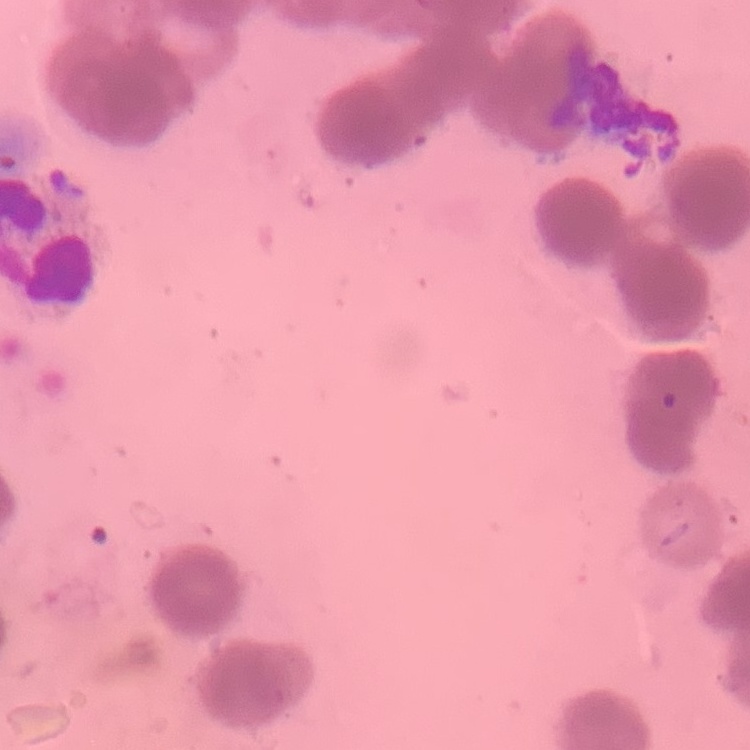 The red blood cells exhibit rouleaux formation. Thin peripheral smear. Square crop of a larger photomicrograph. Stained with either Field's or Giemsa.